Assess the morphology of the red blood cells.
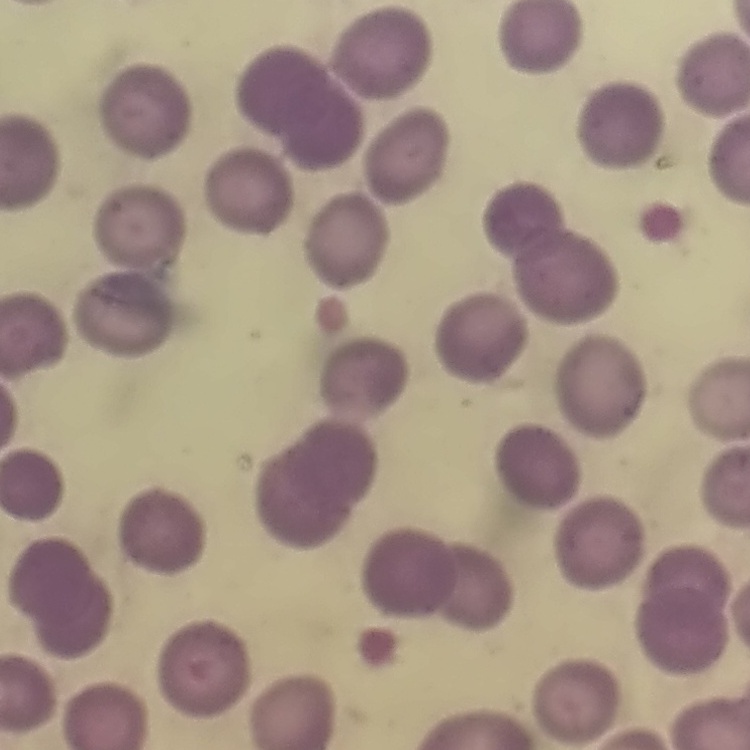

They show no rouleaux formation.

Thin peripheral smear. Field's or Giemsa stain. Square crop of a larger photomicrograph.